Locate every uninfected red blood cell.
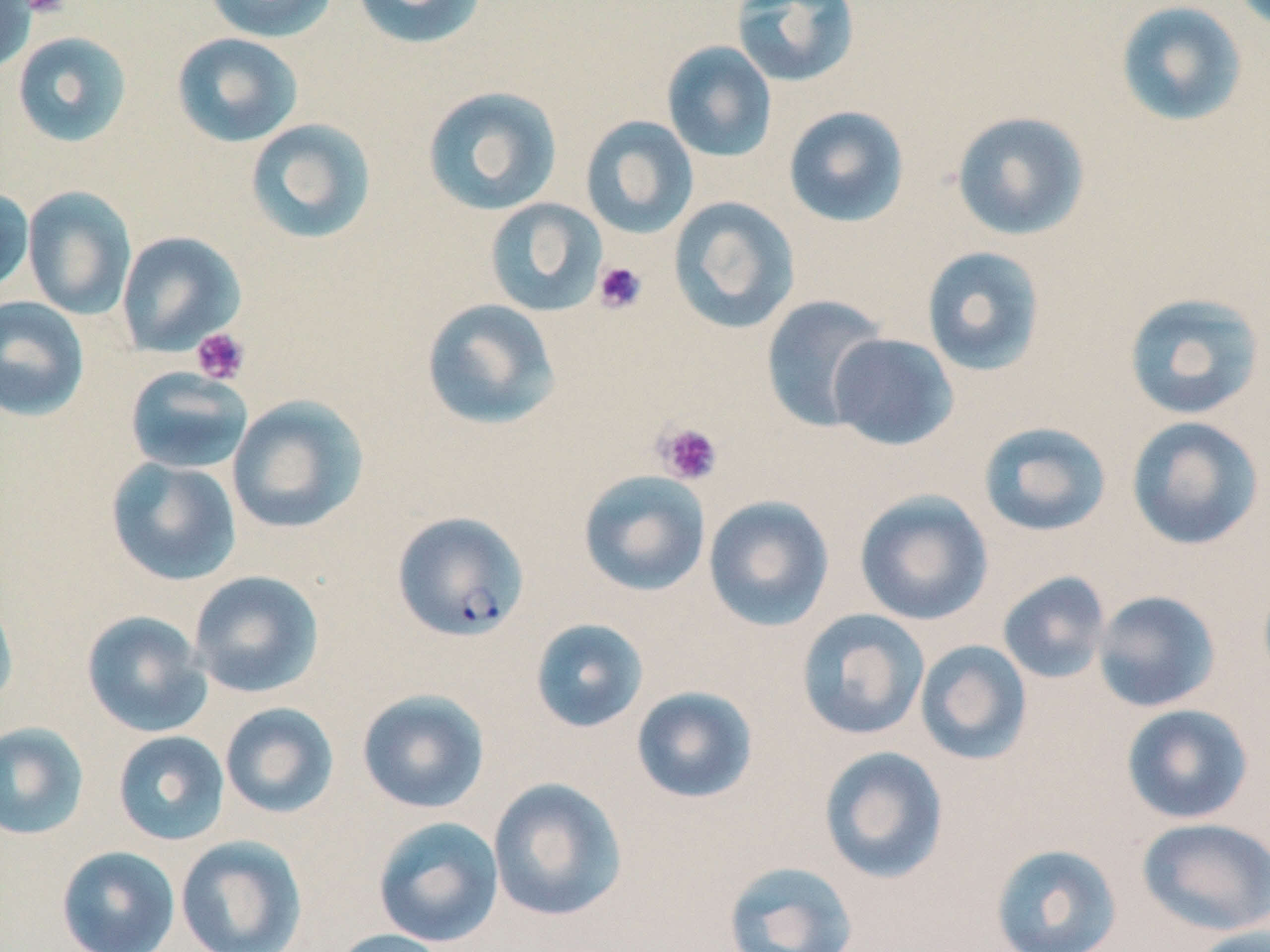
Approximate bounding boxes as (x1,y1)-(x2,y2) corner pairs in pixels.
Uninfected red blood cells: (203,0)-(338,43), (350,0)-(489,50), (0,1)-(36,74), (730,1)-(860,89), (1114,1)-(1248,128), (11,31)-(133,148), (171,32)-(304,147), (661,41)-(778,162), (422,85)-(563,215), (783,105)-(910,228), (951,110)-(1091,241), (580,115)-(699,239), (245,118)-(377,245), (22,185)-(137,320), (0,187)-(35,295), (668,196)-(801,334), (484,197)-(608,317), (115,230)-(246,357), (921,246)-(1046,377), (1123,292)-(1266,420), (760,294)-(889,433), (0,295)-(90,422), (421,298)-(562,431), (827,333)-(959,451), (125,366)-(254,474), (227,395)-(370,535), (1125,416)-(1264,551), (978,421)-(1112,537), (105,457)-(242,586), (577,470)-(712,597), (854,490)-(994,626), (702,495)-(834,632), (188,570)-(324,698), (997,571)-(1111,685), (0,589)-(18,713), (1092,590)-(1222,713), (795,609)-(930,741), (81,610)-(212,738), (530,618)-(649,733), (914,639)-(1033,766), (631,686)-(759,804), (356,688)-(490,814), (219,702)-(339,819), (1120,703)-(1254,825), (0,721)-(90,840), (112,730)-(230,846), (818,745)-(949,884), (487,777)-(629,923), (373,816)-(505,947), (1136,817)-(1269,936), (175,835)-(308,952), (989,843)-(1123,952), (56,845)-(180,952), (722,859)-(859,952), (1186,925)-(1270,952), (327,928)-(454,952).

Plasmodium falciparum-infected red blood cell locations: (391,511)-(530,642). Platelet locations: (21,0)-(70,17), (593,261)-(648,314), (191,327)-(250,385), (654,421)-(723,485). Slide-level diagnosis: Plasmodium falciparum. Captured at 1000x magnification. One field of a larger specimen. May-Grünwald-Giemsa-stained preparation. Image is 1270×952 pixels. Optical microscopy. Thin blood smear.